Report the malaria status of this cell.
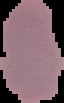

It is uninfected.

Cell region segmented out of the field of view; the surrounding area is masked to black. Image is 64×103 pixels. From a thin blood smear.